Outline each blood parasite and name the species.
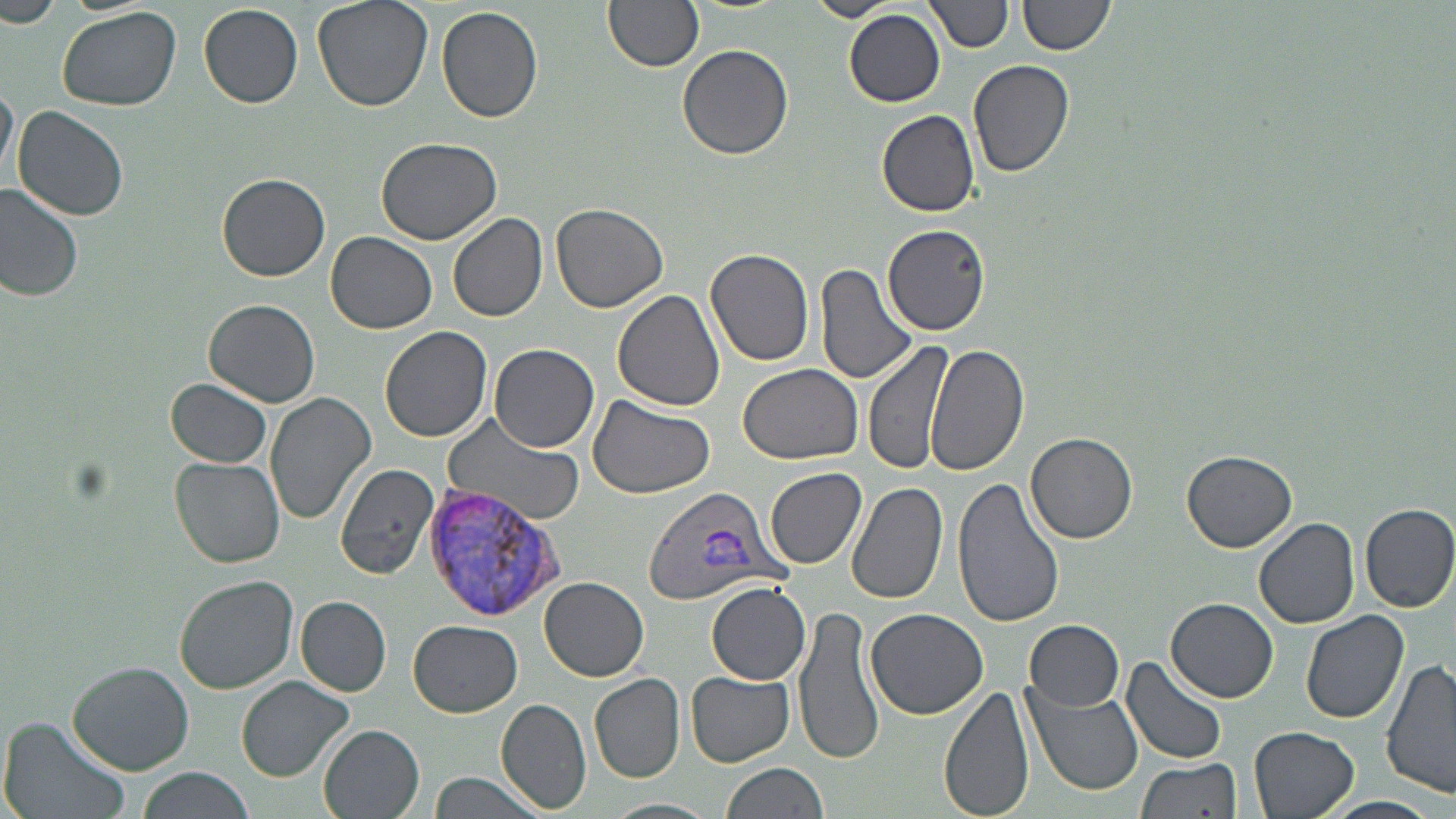

Approximate bounding boxes as (x1, y1, x2, y2) in pixels.
Plasmodium vivax-infected red blood cells: (641, 483, 789, 606), (423, 487, 562, 623).
No Plasmodium falciparum, Plasmodium ovale, Plasmodium malariae, Babesia divergens, or Trypanosoma brucei observed.

Summary:
  - Uninfected red blood cell locations: (0, 0, 64, 30), (311, 0, 431, 112), (604, 0, 704, 72), (806, 0, 896, 23), (927, 0, 1011, 54), (1018, 0, 1114, 57), (56, 4, 182, 111), (199, 4, 303, 107), (436, 6, 543, 123), (845, 9, 945, 108), (678, 45, 794, 162), (967, 60, 1074, 179), (0, 84, 18, 183), (12, 106, 129, 221), (877, 108, 980, 216), (374, 138, 502, 244), (218, 175, 330, 282), (0, 186, 84, 301), (551, 203, 668, 312), (447, 212, 547, 325), (882, 223, 990, 336), (326, 232, 437, 334), (705, 248, 815, 368), (815, 263, 918, 388), (612, 288, 725, 411), (205, 298, 320, 408), (380, 325, 494, 443), (864, 338, 954, 474), (488, 343, 601, 452), (925, 344, 1030, 476), (738, 364, 865, 466), (168, 379, 273, 467), (264, 392, 375, 524), (587, 394, 716, 501), (445, 412, 587, 526), (1027, 432, 1137, 543), (1182, 450, 1296, 552), (170, 455, 286, 568), (333, 466, 441, 582), (768, 468, 867, 569), (952, 477, 1066, 629), (846, 481, 949, 606), (1359, 503, 1456, 612), (1254, 516, 1359, 628), (174, 575, 298, 694), (540, 577, 649, 681), (707, 582, 810, 685), (296, 596, 391, 696), (1168, 598, 1276, 701), (794, 605, 883, 767), (866, 608, 989, 720), (1301, 610, 1409, 726), (409, 620, 523, 717), (1026, 621, 1124, 711), (1121, 654, 1230, 767), (1381, 658, 1456, 799), (67, 661, 195, 774), (1027, 666, 1237, 779), (687, 668, 794, 766), (590, 673, 685, 782), (236, 675, 354, 780), (938, 682, 1036, 819), (1025, 685, 1144, 798), (494, 698, 594, 813), (1, 716, 130, 819), (318, 724, 426, 818), (1249, 726, 1359, 818), (1136, 756, 1241, 819), (722, 761, 831, 819), (136, 768, 255, 819), (429, 772, 548, 818), (1318, 796, 1444, 818), (603, 798, 720, 819)
  - Slide-level diagnosis: Plasmodium vivax
  - Preparation: thin blood film
  - Magnification: 1000x
  - Field of view: single
  - Image size: 1456×819 pixels
  - Stain: May-Grünwald-Giemsa
  - Modality: light microscopy